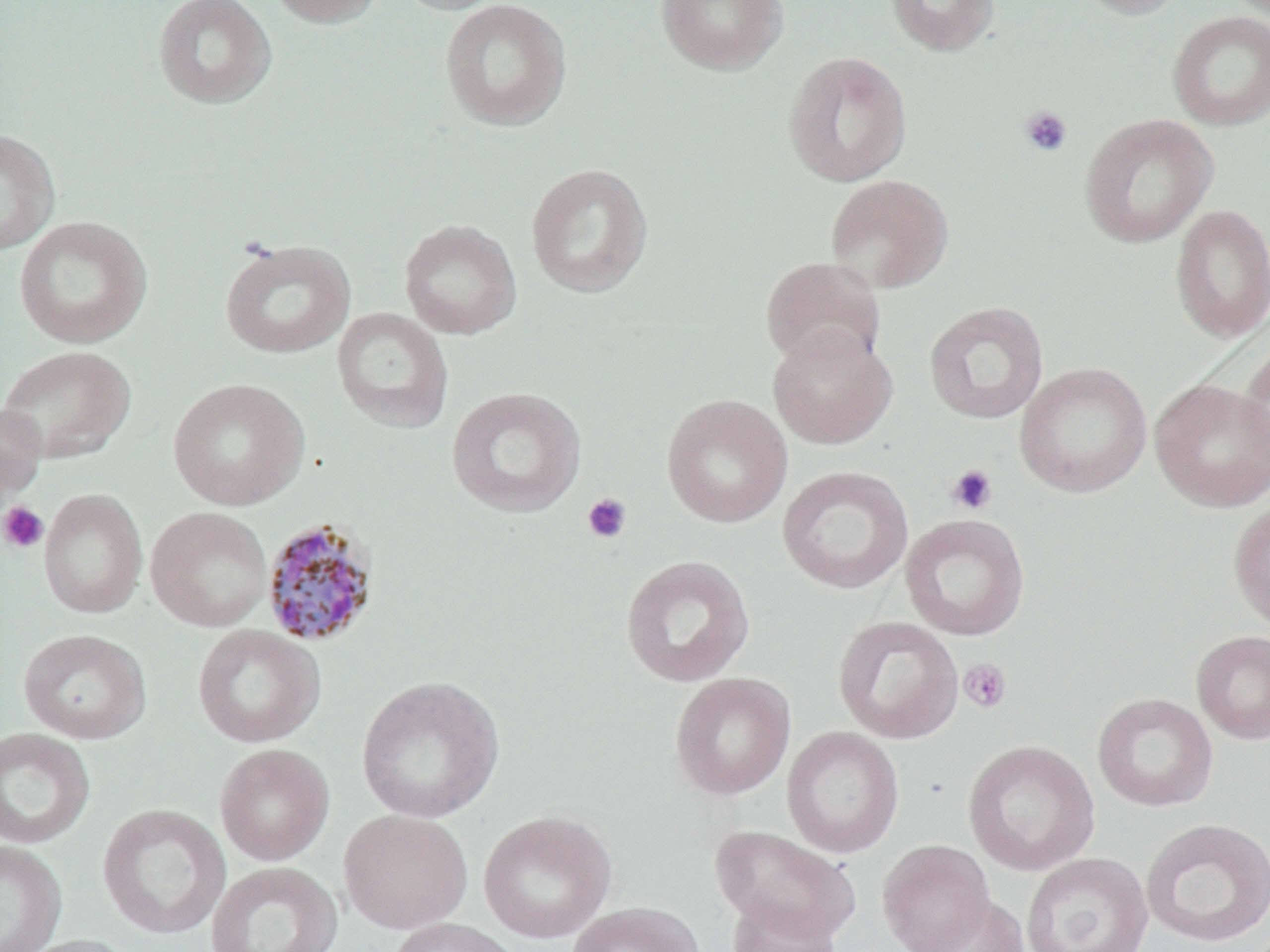
slide-level diagnosis = Plasmodium malariae
preparation = thin blood film
stain = May-Grünwald-Giemsa
image size = 1270×952 pixels
field of view = single
magnification = 1000x
uninfected red blood cell locations = approximate bounding boxes as (x1, y1, x2, y2) in pixels: (152, 0, 277, 109), (265, 0, 385, 28), (390, 0, 512, 15), (439, 0, 573, 131), (655, 0, 789, 75), (885, 0, 1001, 56), (1072, 0, 1191, 19), (1167, 11, 1270, 131), (782, 51, 912, 187), (1078, 113, 1218, 248), (0, 127, 60, 256), (525, 162, 654, 299), (825, 174, 954, 294), (1170, 203, 1269, 343), (12, 214, 153, 349), (398, 219, 522, 339), (219, 238, 356, 360), (760, 255, 887, 370), (924, 301, 1049, 425), (332, 307, 454, 433), (767, 324, 897, 449), (1236, 340, 1270, 474), (0, 345, 136, 465), (1015, 362, 1152, 498), (167, 377, 310, 511), (1150, 378, 1270, 512), (446, 386, 586, 518), (661, 394, 793, 528), (0, 401, 46, 507), (777, 466, 913, 594), (38, 488, 147, 619), (1228, 498, 1270, 632), (145, 506, 273, 632), (900, 514, 1030, 641), (620, 555, 755, 687), (832, 615, 964, 744), (192, 624, 325, 748), (17, 628, 152, 744), (1191, 630, 1270, 744), (670, 672, 796, 800), (355, 674, 505, 824), (1092, 692, 1218, 812), (782, 725, 904, 858), (0, 727, 95, 849), (962, 739, 1100, 876), (214, 743, 335, 866), (97, 804, 231, 940), (338, 809, 474, 934), (477, 810, 616, 943), (1139, 817, 1270, 948), (710, 824, 861, 945), (0, 840, 67, 952), (877, 840, 994, 952), (1021, 852, 1153, 952), (204, 861, 343, 952), (912, 894, 1029, 952), (727, 896, 842, 952), (567, 901, 704, 952), (383, 917, 522, 952), (12, 934, 140, 952)
modality = optical microscopy
platelet locations = approximate bounding boxes as (x1, y1, x2, y2) in pixels: (1018, 105, 1073, 158), (946, 464, 997, 516), (581, 493, 632, 544), (0, 502, 49, 553), (958, 658, 1012, 714)
Plasmodium malariae-infected red blood cell locations = approximate bounding boxes as (x1, y1, x2, y2) in pixels: (260, 518, 381, 648)